Assess this cell for malaria.
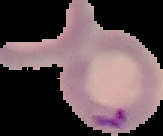

Parasitized.

Summary:
  - Preparation: thin blood smear
  - Image size: 163×136 pixels
  - Image type: cell region segmented out of the field of view; surrounding area masked to black